Describe the morphology of the red blood cells.
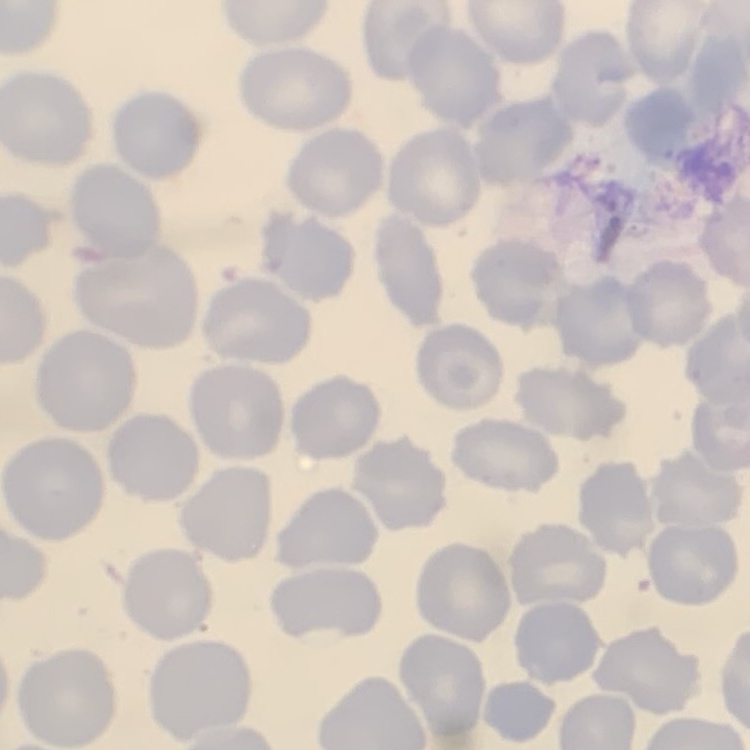
They show no rouleaux formation.

Square crop of a larger photomicrograph. Stained with either Field's or Giemsa. Thin blood smear.